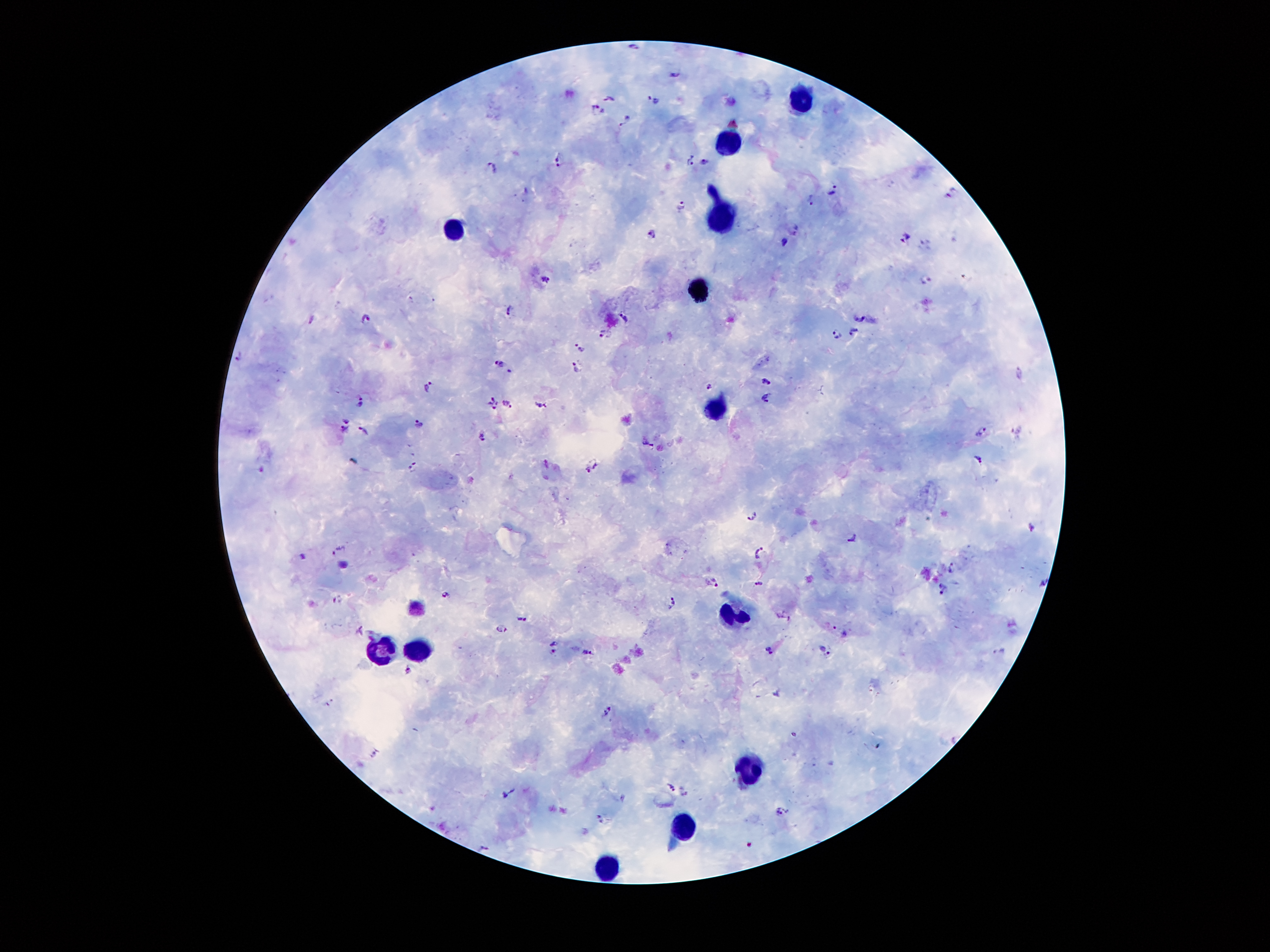
coordinate format = approximate centers as (x, y) in pixels
leukocyte locations = (799, 101), (726, 142), (725, 218), (451, 228), (697, 289), (722, 407), (737, 612), (384, 647), (413, 647), (756, 768), (685, 823), (602, 868)
malaria parasite locations = (633, 47), (675, 74), (610, 98), (653, 99), (598, 110), (626, 120), (558, 161), (691, 161), (703, 161), (493, 167), (832, 189), (952, 192), (811, 201), (681, 205), (651, 233), (904, 237), (784, 242), (966, 276), (925, 279), (545, 280), (508, 309), (858, 315), (623, 317), (312, 319), (365, 319), (854, 331), (605, 334), (836, 334), (581, 349), (241, 356), (500, 364), (578, 368), (511, 372), (1018, 373), (767, 380), (709, 385), (426, 386), (766, 397), (490, 399), (363, 403), (507, 404), (540, 404), (495, 405), (347, 420), (417, 425), (344, 429), (364, 430), (980, 431), (1016, 432), (483, 436), (648, 441), (979, 459), (548, 463), (595, 465), (414, 467), (586, 471), (753, 515), (1032, 528), (853, 538), (337, 549), (759, 551), (303, 557), (951, 567), (712, 581), (1043, 582), (759, 585), (942, 590), (445, 595), (337, 599), (672, 602), (520, 616), (501, 628), (840, 630), (554, 647), (586, 651), (769, 651), (824, 651), (998, 651), (408, 669), (776, 694), (331, 703), (607, 710), (376, 756), (671, 788), (509, 792), (684, 793), (781, 812), (602, 819), (484, 848)
magnification = 100x
image size = 1270×952 pixels
field of view = single
capture = smartphone camera through the microscope eyepiece
patient malaria status = infected with Plasmodium falciparum
stain = Giemsa
preparation = thick peripheral-blood smear